Report the malaria status of this cell.
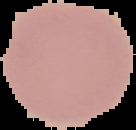

Uninfected.

Cell region segmented out of the field of view; the surrounding area is masked to black. From a thin blood film. Image is 136×130 pixels.